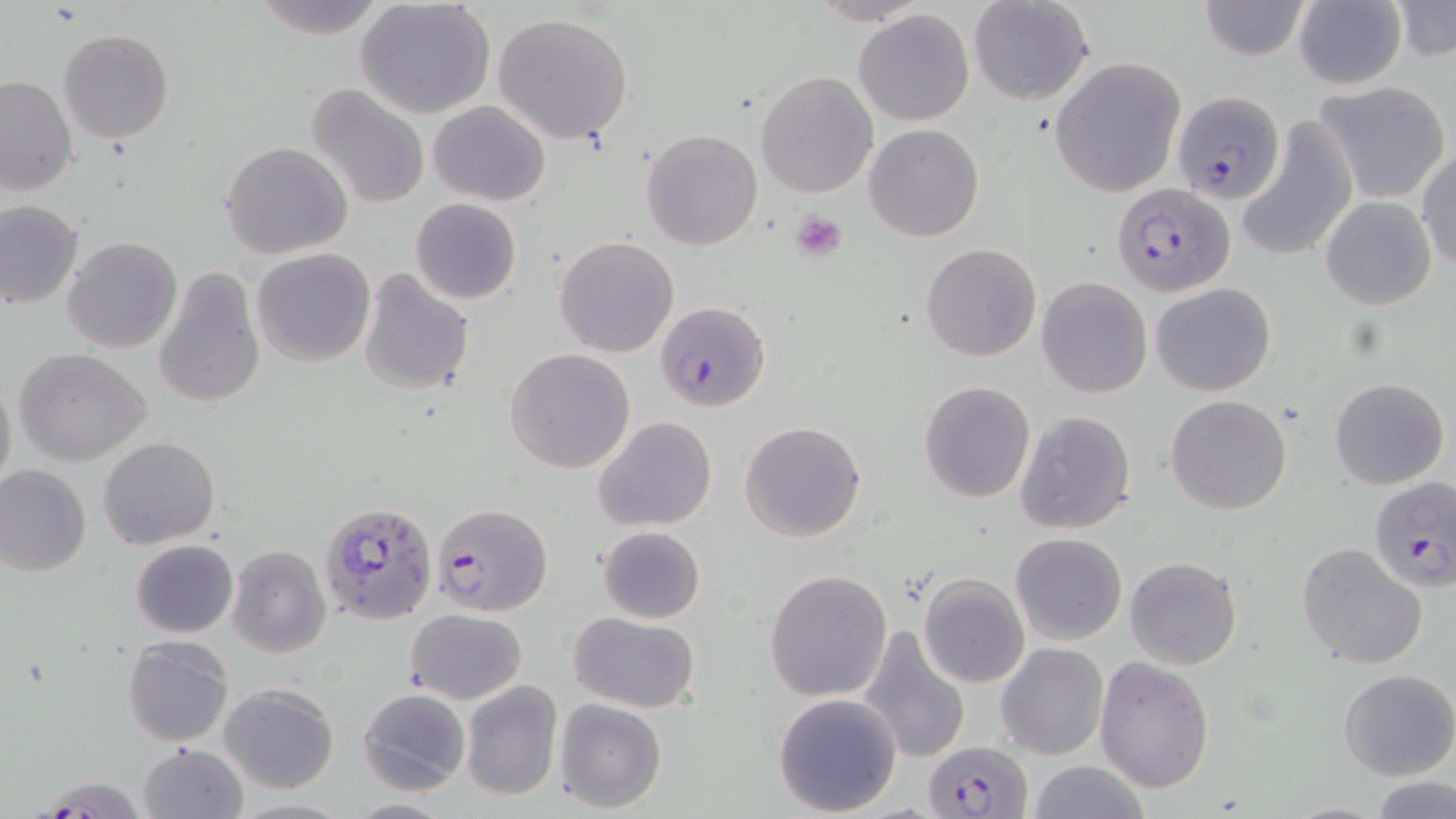
Summary:
  - Coordinate format: approximate bounding boxes as named x1/y1/x2/y2 corners in pixels
  - Platelet locations: (x1=790, y1=211, x2=847, y2=263)
  - Plasmodium falciparum-infected red blood cell locations: (x1=1172, y1=90, x2=1288, y2=206), (x1=1111, y1=182, x2=1233, y2=297), (x1=656, y1=301, x2=771, y2=413), (x1=1368, y1=477, x2=1456, y2=590), (x1=319, y1=501, x2=437, y2=627), (x1=432, y1=503, x2=552, y2=618), (x1=923, y1=741, x2=1032, y2=817)
  - Uninfected red blood cell locations: (x1=355, y1=0, x2=497, y2=119), (x1=968, y1=0, x2=1093, y2=106), (x1=1196, y1=0, x2=1312, y2=61), (x1=1292, y1=0, x2=1408, y2=90), (x1=246, y1=1, x2=389, y2=38), (x1=1390, y1=2, x2=1455, y2=64), (x1=853, y1=9, x2=975, y2=126), (x1=491, y1=13, x2=634, y2=142), (x1=58, y1=29, x2=176, y2=145), (x1=1049, y1=59, x2=1185, y2=197), (x1=755, y1=71, x2=879, y2=198), (x1=1, y1=74, x2=76, y2=197), (x1=1311, y1=81, x2=1451, y2=205), (x1=306, y1=83, x2=431, y2=210), (x1=428, y1=102, x2=550, y2=205), (x1=1238, y1=117, x2=1358, y2=261), (x1=865, y1=123, x2=983, y2=242), (x1=642, y1=128, x2=764, y2=250), (x1=221, y1=142, x2=353, y2=260), (x1=1416, y1=148, x2=1455, y2=270), (x1=1319, y1=195, x2=1436, y2=309), (x1=410, y1=197, x2=522, y2=305), (x1=0, y1=199, x2=83, y2=310), (x1=63, y1=236, x2=182, y2=354), (x1=553, y1=236, x2=679, y2=358), (x1=920, y1=243, x2=1042, y2=362), (x1=252, y1=248, x2=376, y2=367), (x1=153, y1=265, x2=266, y2=408), (x1=357, y1=268, x2=475, y2=396), (x1=1036, y1=277, x2=1153, y2=397), (x1=1149, y1=281, x2=1276, y2=397), (x1=14, y1=347, x2=152, y2=465), (x1=505, y1=348, x2=636, y2=473), (x1=0, y1=370, x2=15, y2=496), (x1=1330, y1=378, x2=1449, y2=488), (x1=918, y1=380, x2=1035, y2=503), (x1=1165, y1=394, x2=1291, y2=515), (x1=1013, y1=409, x2=1139, y2=535), (x1=593, y1=417, x2=716, y2=533), (x1=739, y1=420, x2=867, y2=543), (x1=99, y1=435, x2=220, y2=549), (x1=0, y1=466, x2=91, y2=578), (x1=596, y1=525, x2=705, y2=624), (x1=1010, y1=533, x2=1127, y2=645), (x1=131, y1=539, x2=238, y2=637), (x1=1296, y1=542, x2=1428, y2=670), (x1=227, y1=545, x2=331, y2=658), (x1=1124, y1=556, x2=1242, y2=670), (x1=763, y1=570, x2=892, y2=701), (x1=917, y1=574, x2=1030, y2=687), (x1=406, y1=609, x2=527, y2=704), (x1=568, y1=612, x2=700, y2=713), (x1=858, y1=625, x2=972, y2=764), (x1=122, y1=635, x2=234, y2=746), (x1=995, y1=643, x2=1108, y2=761), (x1=1095, y1=657, x2=1215, y2=793), (x1=1339, y1=668, x2=1455, y2=781), (x1=461, y1=680, x2=563, y2=801), (x1=219, y1=683, x2=339, y2=794), (x1=475, y1=685, x2=653, y2=804), (x1=358, y1=688, x2=470, y2=796), (x1=772, y1=693, x2=903, y2=816), (x1=554, y1=698, x2=668, y2=814), (x1=137, y1=742, x2=247, y2=819), (x1=1026, y1=761, x2=1151, y2=819), (x1=36, y1=775, x2=148, y2=816), (x1=1371, y1=776, x2=1455, y2=819), (x1=341, y1=798, x2=455, y2=817)
  - Slide-level diagnosis: Plasmodium falciparum
  - Magnification: 1000x
  - Image size: 1456×819 pixels
  - Modality: optical microscopy
  - Preparation: thin blood smear
  - Stain: May-Grünwald-Giemsa
  - Field of view: one of a larger specimen